Locate every blood parasite and identify its species.
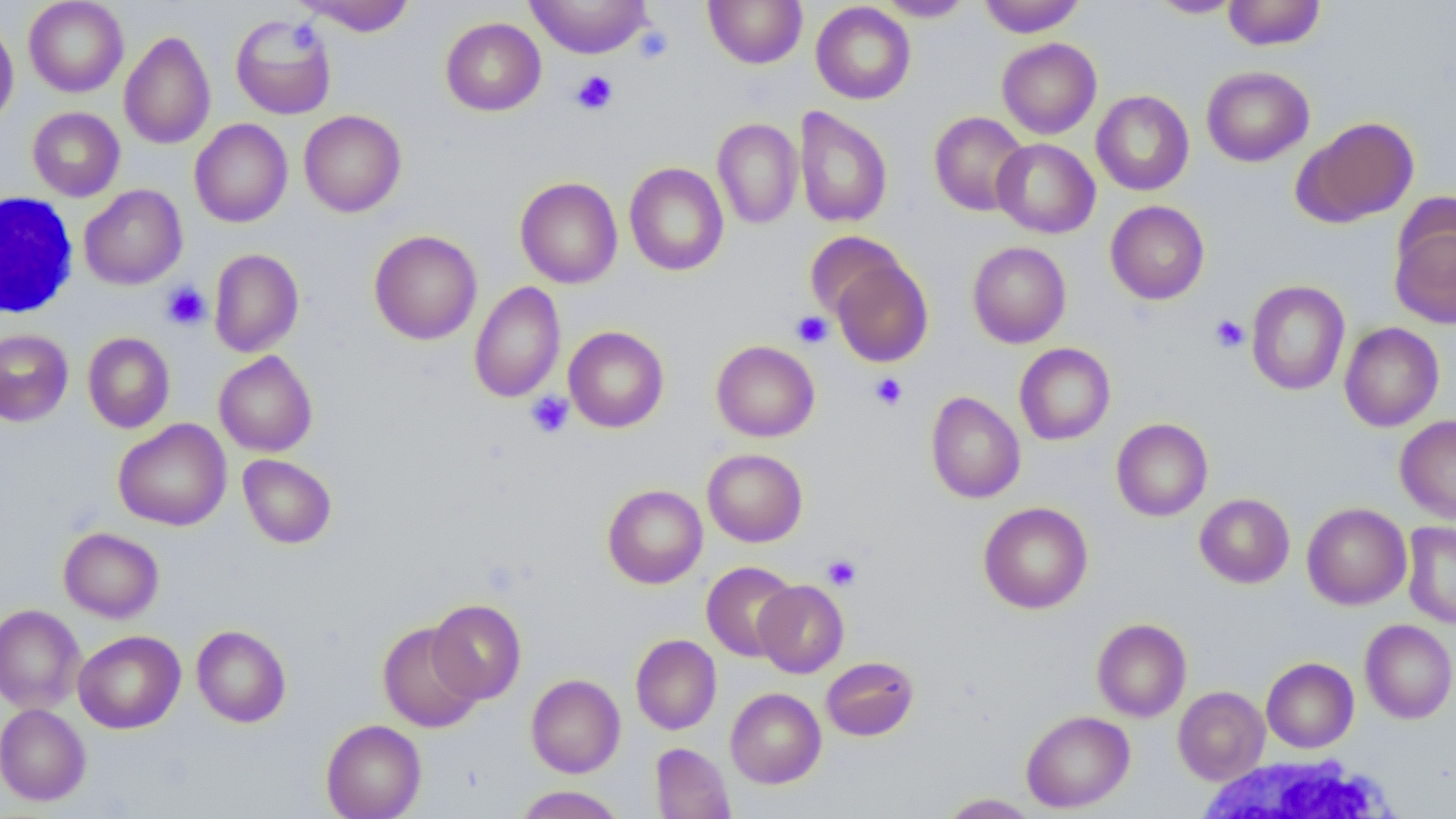
No blood parasites observed.

Approximate bounding boxes as (x1, y1, x2, y2) in pixels. White blood cell locations: (0, 192, 79, 320), (1193, 753, 1403, 819). Uninfected red blood cell locations: (24, 0, 128, 97), (295, 0, 417, 36), (526, 0, 652, 58), (703, 0, 807, 68), (873, 0, 975, 21), (978, 0, 1086, 37), (1147, 0, 1245, 18), (1222, 0, 1326, 50), (811, 2, 916, 105), (230, 14, 337, 120), (440, 17, 546, 116), (0, 19, 19, 127), (119, 30, 215, 149), (997, 38, 1101, 139), (1201, 65, 1314, 166), (1092, 90, 1194, 195), (27, 106, 125, 201), (794, 106, 893, 228), (299, 110, 406, 217), (929, 112, 1030, 217), (1294, 116, 1419, 228), (712, 118, 802, 229), (190, 119, 293, 227), (992, 138, 1099, 238), (625, 162, 729, 276), (515, 177, 623, 289), (79, 185, 188, 289), (1105, 200, 1210, 305), (1390, 213, 1456, 329), (369, 230, 482, 344), (805, 231, 905, 320), (967, 241, 1071, 347), (209, 249, 304, 357), (831, 259, 933, 367), (1246, 280, 1350, 396), (469, 281, 565, 403), (1340, 322, 1444, 431), (564, 326, 669, 432), (0, 329, 74, 426), (83, 332, 175, 433), (711, 340, 820, 442), (1015, 343, 1115, 445), (214, 350, 318, 456), (925, 391, 1025, 503), (1395, 415, 1456, 524), (1111, 418, 1212, 521), (113, 419, 231, 531), (702, 448, 808, 547), (238, 454, 337, 549), (602, 484, 707, 588), (1195, 493, 1294, 588), (978, 502, 1093, 614), (1302, 503, 1411, 610), (1402, 521, 1456, 629), (58, 527, 164, 622), (701, 561, 798, 662), (754, 580, 849, 678), (427, 598, 526, 704), (0, 604, 85, 713), (1092, 618, 1191, 722), (1360, 619, 1456, 724), (378, 623, 482, 733), (191, 625, 291, 727), (73, 630, 186, 733), (630, 634, 721, 735), (821, 656, 919, 741), (1261, 657, 1359, 753), (526, 674, 625, 778), (1173, 686, 1270, 784), (725, 687, 826, 788), (0, 703, 90, 806), (1021, 710, 1135, 812), (321, 719, 426, 819), (651, 742, 735, 819), (514, 786, 625, 819), (938, 793, 1039, 818). Platelet locations: (632, 25, 673, 65), (571, 70, 618, 115), (161, 282, 210, 330), (792, 311, 833, 348), (1210, 314, 1249, 353), (869, 373, 907, 410), (526, 391, 574, 438), (822, 554, 862, 591). Slide-level diagnosis: negative for blood parasites. Optical microscopy. Image is 1456×819 pixels. One field of a larger specimen. 1000x magnification. Thin blood film. May-Grünwald-Giemsa-stained preparation.